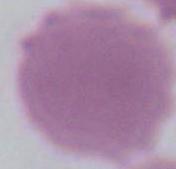

Photomicrograph. A red blood cell is shown. Captured at 1000x magnification.